Assess this cell for malaria.
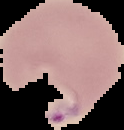

It is parasitized.

Image is 124×130 pixels. Cell region segmented out of the field of view; the surrounding area is masked to black. From a thin blood film.